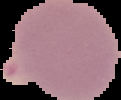 Segmented cell region on a black background. Image is 121×100 pixels. Malaria status: uninfected. From a thin blood film.